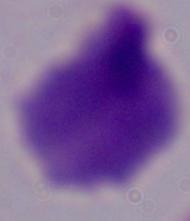
Captured at 1000x magnification. A trichomonad is shown. Photomicrograph.